State which cell type is depicted.
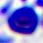

A leukocyte.

Summary:
  - Magnification: 400x
  - Modality: micrograph